State which parasite is depicted.
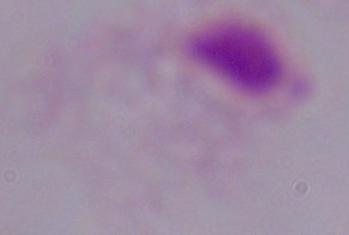

This is a trichomonad.

magnification: 1000x
modality: micrograph